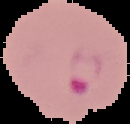
From a thin blood smear. Result: Plasmodium parasites detected. Image is 130×124 pixels. Cell region segmented out of the field of view; the surrounding area is masked to black.